Locate and identify every blood parasite.
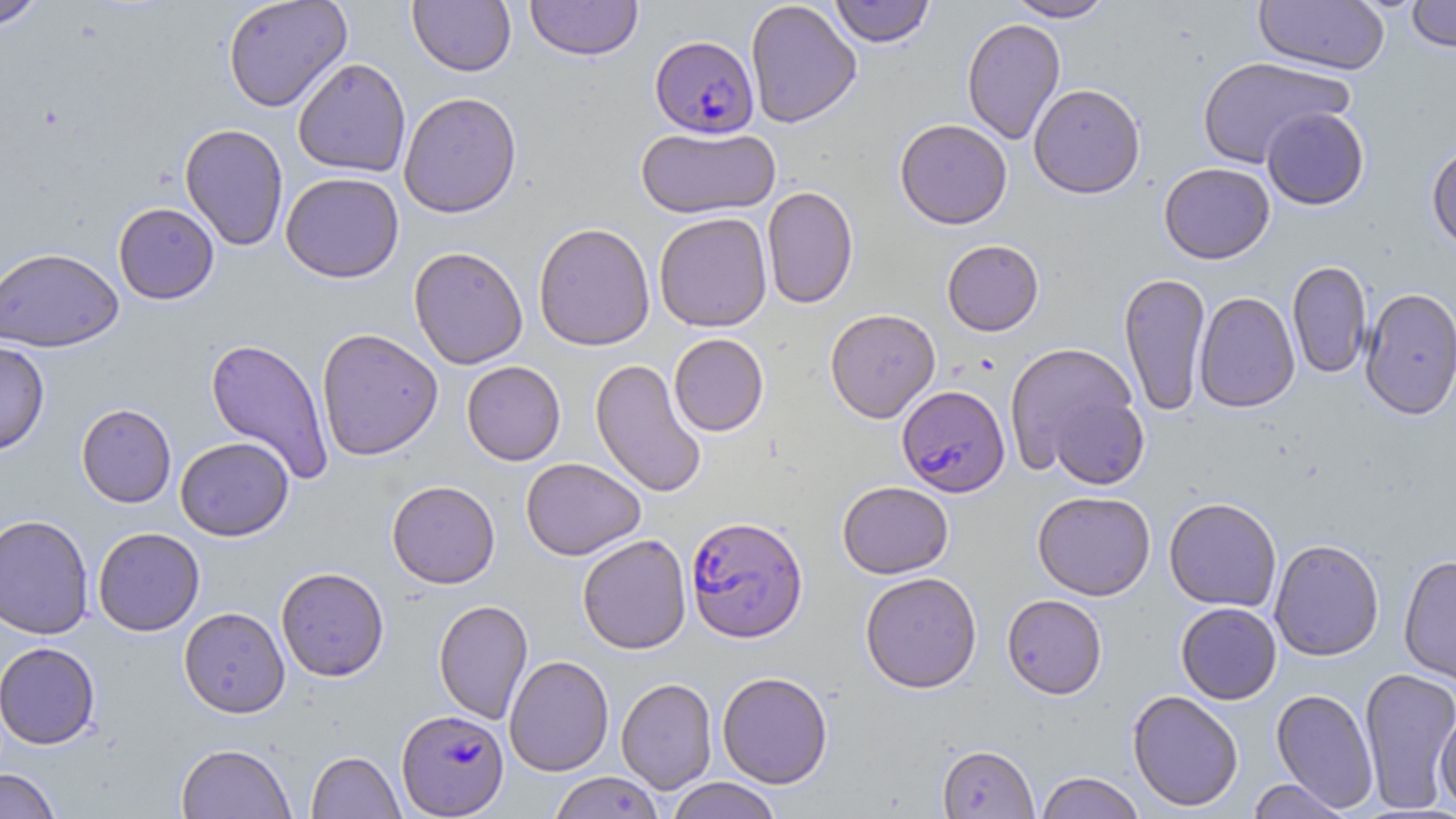

Approximate bounding boxes as (x1,y1)-(x2,y2) corner pairs in pixels.
Plasmodium falciparum-infected red blood cells: (650,34)-(759,138), (897,384)-(1010,497), (686,515)-(808,643), (396,709)-(508,817).
No Plasmodium ovale, Plasmodium malariae, Plasmodium vivax, Babesia divergens, or Trypanosoma brucei observed.

Summary:
  - Uninfected red blood cell locations: (0,0)-(46,31), (222,0)-(352,112), (408,0)-(516,76), (525,0)-(643,61), (745,0)-(862,129), (828,0)-(936,47), (1005,0)-(1116,22), (1253,0)-(1390,75), (1405,0)-(1456,52), (961,18)-(1066,145), (1197,56)-(1352,169), (292,58)-(411,177), (1029,83)-(1145,199), (398,91)-(522,218), (1261,107)-(1370,210), (895,118)-(1012,229), (179,123)-(289,251), (636,126)-(781,218), (1426,141)-(1456,252), (1158,162)-(1275,264), (281,172)-(405,283), (762,186)-(858,309), (113,202)-(220,304), (654,212)-(773,332), (533,222)-(655,351), (941,239)-(1044,336), (0,246)-(124,352), (408,246)-(528,369), (1287,260)-(1371,379), (1118,272)-(1211,415), (1359,287)-(1456,420), (1194,291)-(1300,412), (825,308)-(941,423), (316,327)-(443,461), (668,333)-(769,436), (205,338)-(335,485), (0,341)-(50,454), (1004,342)-(1141,476), (590,358)-(707,498), (461,361)-(566,466), (1046,390)-(1150,490), (76,403)-(177,508), (174,436)-(294,541), (521,457)-(645,560), (386,480)-(500,589), (837,481)-(954,578), (1032,490)-(1156,601), (1164,497)-(1282,611), (0,514)-(94,639), (93,527)-(205,636), (577,534)-(692,654), (1269,538)-(1384,661), (1398,555)-(1456,685), (275,566)-(390,681), (860,572)-(982,693), (1002,594)-(1107,699), (433,599)-(533,724), (1175,602)-(1281,704), (178,606)-(290,718), (0,642)-(101,749), (504,655)-(614,776), (1359,667)-(1456,813), (717,671)-(833,788), (505,672)-(716,785), (616,677)-(717,794), (1271,688)-(1379,813), (1127,690)-(1244,811), (1434,710)-(1456,813), (175,742)-(296,818), (937,744)-(1039,818), (306,751)-(405,818), (0,768)-(62,819), (1035,771)-(1145,819), (548,772)-(664,819), (665,777)-(783,819), (1247,778)-(1352,818)
  - Slide-level diagnosis: Plasmodium falciparum
  - Stain: May-Grünwald-Giemsa
  - Image size: 1456×819 pixels
  - Preparation: thin blood film
  - Field of view: single
  - Modality: light microscopy
  - Magnification: 1000x